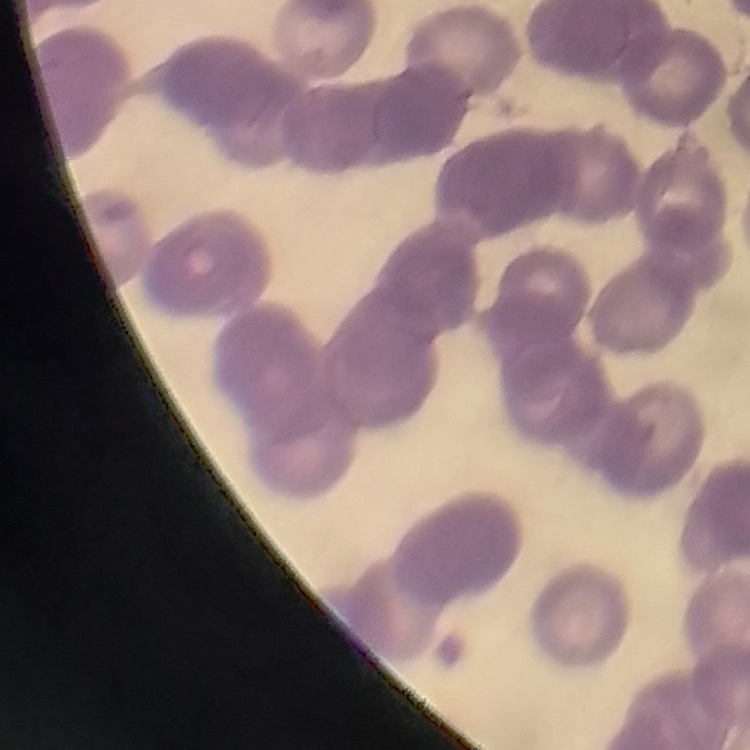

red blood cell morphology = rouleaux formation
image type = one tile cut from a larger photomicrograph
preparation = thin peripheral smear
stain = Field's or Giemsa